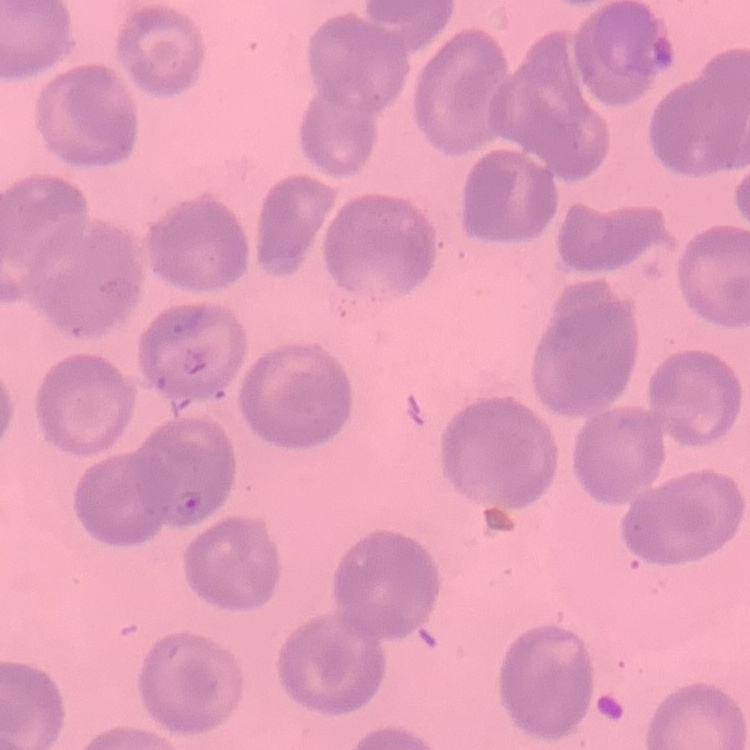
The erythrocytes exhibit no rouleaux formation. One tile cut from a larger photomicrograph. Field's or Giemsa stain. Thin blood smear.